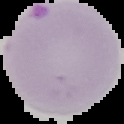
Malaria status: parasitized. From a thin blood film. Image is 124×124 pixels. The area outside the segmented cell region is set to black.